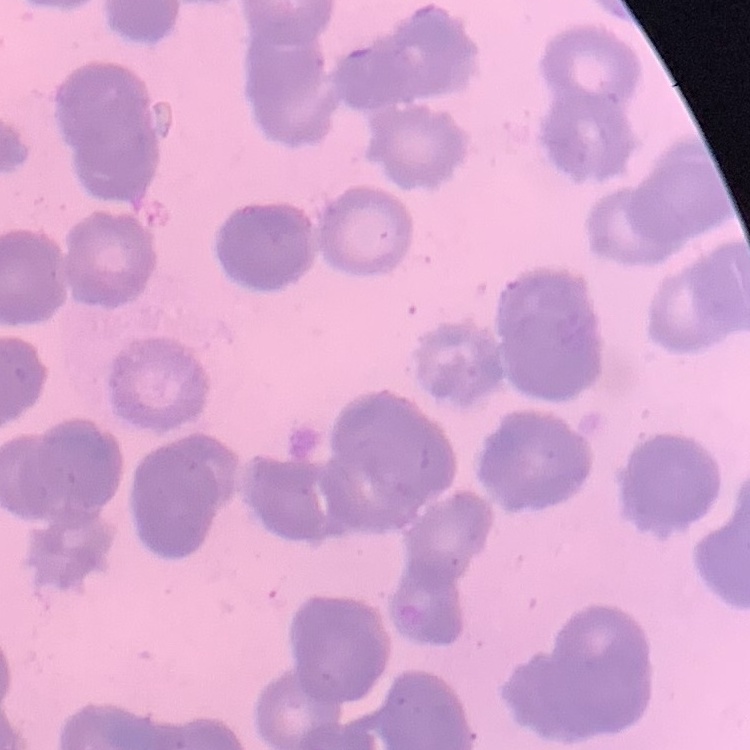
red blood cell morphology = rouleaux formation
preparation = thin blood smear
stain = Field's or Giemsa
image type = one tile cut from a larger photomicrograph